Assess this cell for malaria.
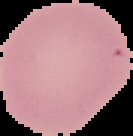

It is uninfected.

Summary:
  - Preparation: thin blood smear
  - Image size: 133×136 pixels
  - Image type: cell region segmented out of the field of view; surrounding area masked to black